Locate and identify every blood parasite.
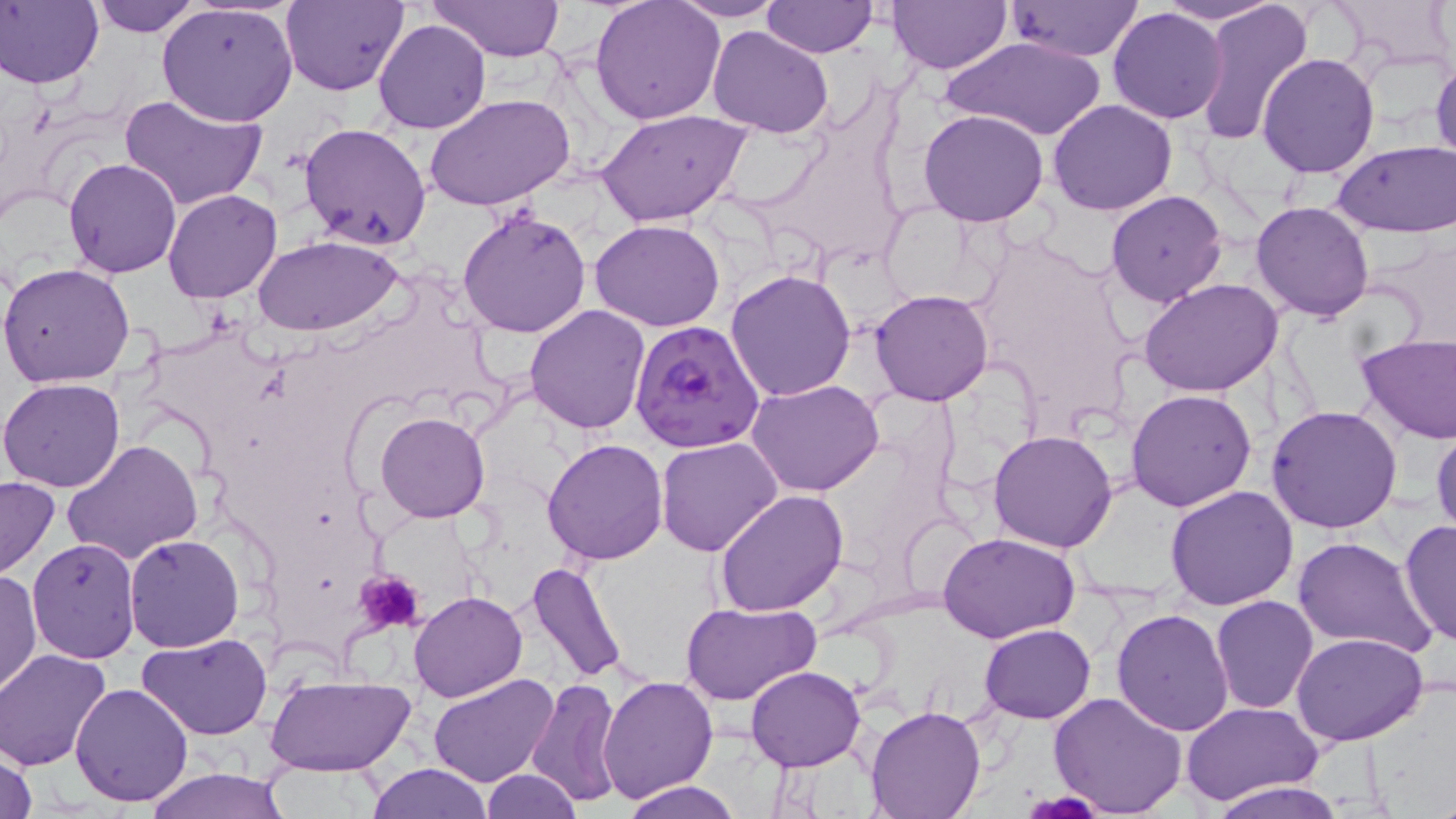
Approximate bounding boxes as (x1,y1)-(x2,y2) corner pairs in pixels.
Plasmodium falciparum-infected red blood cells: (629,319)-(764,454).
No Plasmodium ovale, Plasmodium malariae, Plasmodium vivax, Babesia divergens, or Trypanosoma brucei observed.

Summary:
  - Uninfected red blood cell locations: (89,0)-(200,37), (281,0)-(407,94), (432,0)-(565,63), (590,0)-(725,125), (764,0)-(875,58), (1153,0)-(1282,25), (1331,0)-(1455,71), (1,1)-(103,89), (667,1)-(791,22), (888,1)-(1010,72), (1192,1)-(1313,144), (1005,2)-(1145,60), (157,3)-(298,126), (1107,8)-(1228,124), (373,18)-(490,134), (707,25)-(834,138), (940,33)-(1107,141), (377,42)-(527,176), (1258,52)-(1380,177), (1430,58)-(1456,170), (119,90)-(267,211), (424,92)-(574,210), (1048,99)-(1177,216), (597,108)-(752,227), (918,109)-(1050,227), (299,121)-(433,249), (1333,141)-(1456,234), (64,158)-(181,278), (162,189)-(283,304), (1105,189)-(1227,307), (1120,193)-(1254,393), (876,201)-(991,307), (1251,201)-(1374,322), (457,207)-(592,339), (591,220)-(727,332), (254,234)-(404,335), (0,262)-(135,388), (726,269)-(857,401), (1139,279)-(1285,398), (870,289)-(995,406), (525,304)-(651,433), (1357,332)-(1456,445), (1,376)-(127,493), (746,378)-(884,496), (1126,390)-(1257,512), (1266,406)-(1403,534), (375,411)-(489,522), (1431,426)-(1455,538), (988,430)-(1119,552), (657,435)-(782,556), (63,439)-(203,564), (541,439)-(668,564), (0,476)-(59,577), (1164,485)-(1299,610), (715,489)-(848,615), (1398,520)-(1456,649), (938,532)-(1082,641), (124,533)-(244,652), (1289,536)-(1435,660), (26,538)-(141,664), (526,560)-(628,686), (0,569)-(41,697), (409,590)-(526,702), (1210,594)-(1319,714), (682,601)-(820,705), (1112,608)-(1234,736), (979,624)-(1095,722), (139,632)-(272,741), (1292,634)-(1426,747), (1,649)-(113,769), (745,665)-(864,772), (428,672)-(558,788), (597,672)-(718,801), (265,674)-(413,778), (528,677)-(622,808), (69,680)-(194,806), (1047,691)-(1186,817), (1181,701)-(1320,807), (864,706)-(985,819), (0,745)-(38,819), (366,762)-(494,818), (143,768)-(291,819), (479,769)-(581,818), (621,780)-(741,819), (1204,780)-(1354,818)
  - Platelet locations: (356,570)-(425,633)
  - Slide-level diagnosis: Plasmodium falciparum
  - Field of view: single
  - Image size: 1456×819 pixels
  - Magnification: 1000x
  - Stain: May-Grünwald-Giemsa
  - Preparation: thin blood smear
  - Modality: optical microscopy